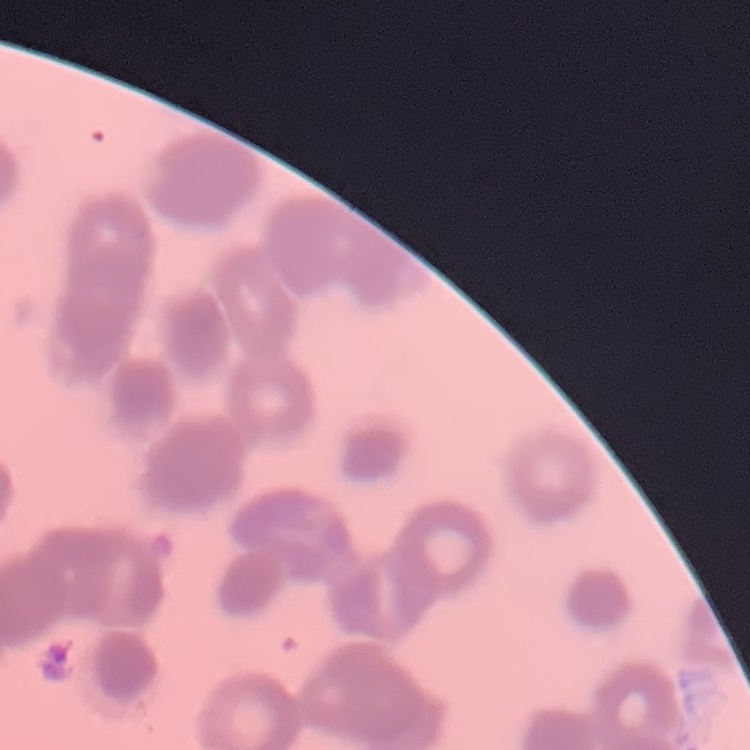

erythrocyte morphology = rouleaux formation
image type = one tile cut from a larger photomicrograph
stain = Field's or Giemsa
preparation = thin blood smear